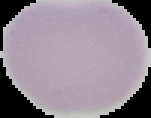
result = no malaria parasites detected
preparation = thin blood smear
image type = segmented cell region with the area outside set to black
image size = 151×118 pixels